Identify the parasite.
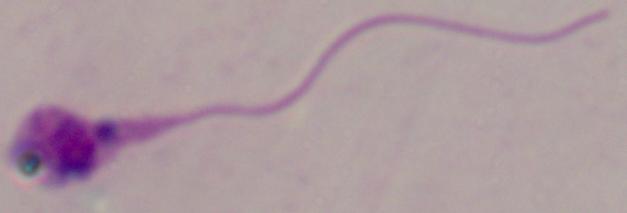
Leishmania.

1000x magnification. Micrograph.